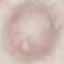
malaria status = uninfected
preparation = thin smear
stain = Giemsa
capture = smartphone camera at the microscope eyepiece
image type = automatically extracted cell patch, resized to 64 × 64 pixels